Report the malaria status of this cell.
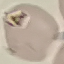

It is uninfected.

capture: smartphone through the microscope eyepiece
preparation: thin blood film
stain: Giemsa
image_type: cell patch, automatically extracted from a larger field of view and resized to 64 × 64 pixels